Outline each blood parasite and name the species.
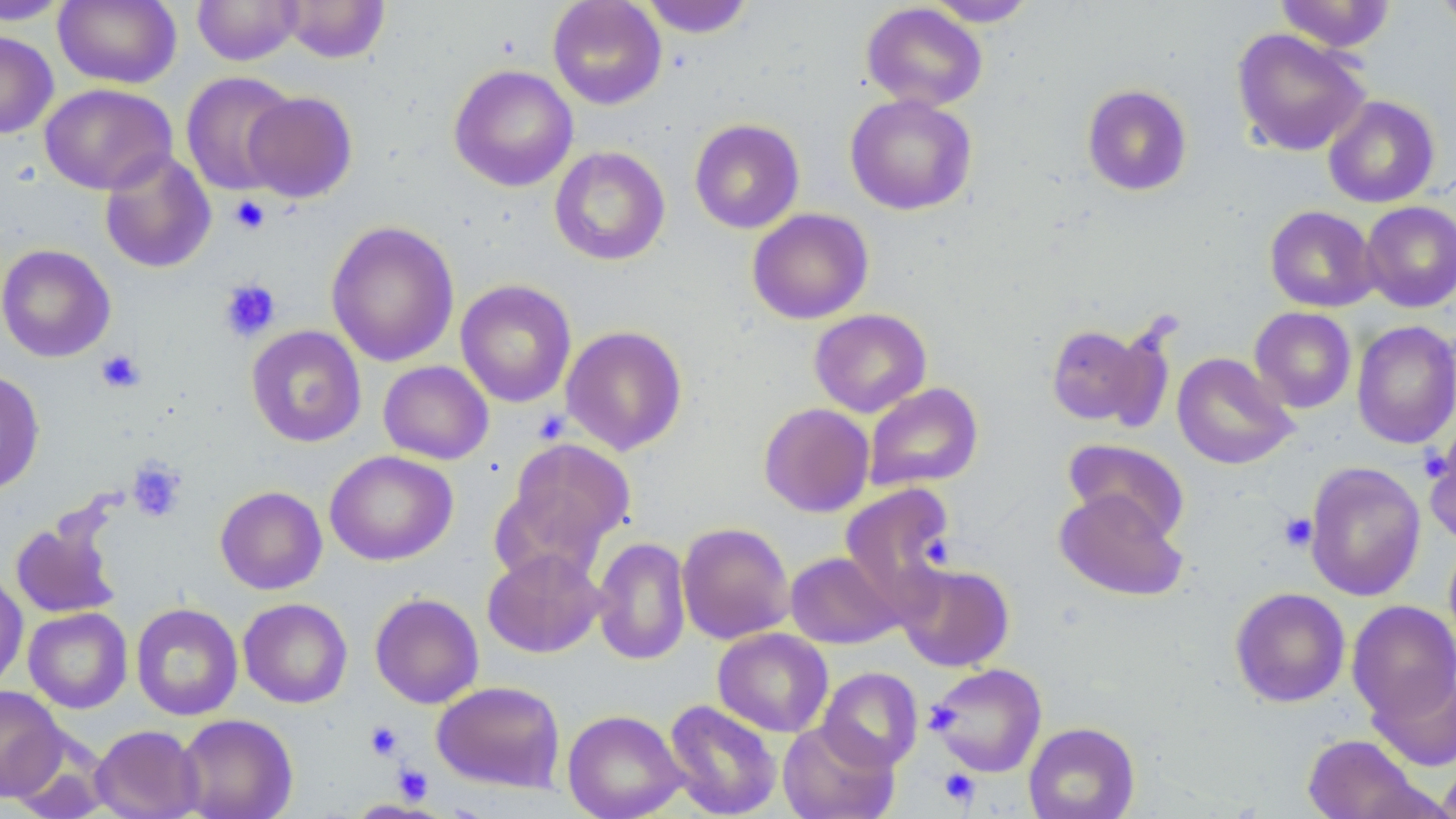

No blood parasites observed.

slide-level diagnosis = no evidence of blood parasites
platelet locations = approximate bounding boxes as (x1,y1)-(x2,y2) corner pairs in pixels: (229,196)-(271,235), (218,279)-(281,342), (96,349)-(144,394), (127,459)-(186,522), (1279,512)-(1318,552), (922,533)-(955,567), (365,720)-(404,761), (393,764)-(432,803), (938,769)-(980,808)
magnification = 1000x
uninfected red blood cell locations = approximate bounding boxes as (x1,y1)-(x2,y2) corner pairs in pixels: (54,0)-(181,88), (192,0)-(303,66), (280,0)-(390,63), (547,0)-(666,109), (638,0)-(755,38), (923,0)-(1040,26), (1275,0)-(1396,52), (1434,0)-(1456,32), (0,1)-(74,25), (861,3)-(988,111), (1231,28)-(1369,156), (0,30)-(58,139), (449,65)-(578,192), (181,71)-(298,196), (1081,83)-(1193,196), (39,84)-(178,195), (243,91)-(358,203), (845,93)-(977,215), (1322,95)-(1440,208), (689,118)-(804,234), (549,146)-(670,266), (99,150)-(216,274), (1360,201)-(1456,312), (1264,205)-(1379,312), (747,208)-(874,324), (326,221)-(460,367), (0,243)-(115,363), (455,280)-(577,407), (1249,307)-(1356,413), (809,308)-(931,417), (1351,320)-(1456,449), (1044,322)-(1168,429), (561,324)-(688,455), (246,325)-(367,447), (1172,352)-(1298,470), (378,360)-(494,465), (0,369)-(45,494), (864,382)-(984,491), (758,402)-(874,517), (1423,427)-(1456,545), (504,437)-(636,558), (1063,439)-(1190,542), (325,450)-(458,566), (1304,461)-(1426,602), (839,483)-(955,608), (215,486)-(327,595), (1054,489)-(1188,602), (10,515)-(122,620), (677,522)-(795,644), (592,537)-(691,666), (1444,537)-(1456,652), (482,548)-(605,658), (785,552)-(903,649), (896,562)-(1014,672), (0,570)-(28,691), (1229,587)-(1350,708), (369,592)-(484,708), (238,598)-(352,708), (1346,600)-(1456,721), (130,602)-(243,721), (24,607)-(133,713), (713,627)-(833,737), (926,662)-(1047,777), (818,667)-(923,771), (1368,668)-(1456,772), (431,680)-(565,792), (1,685)-(67,802), (663,699)-(782,819), (562,709)-(687,819), (175,713)-(298,819), (778,720)-(899,819), (1024,721)-(1140,819), (90,725)-(204,819), (6,733)-(115,818), (1302,734)-(1426,819), (1438,757)-(1456,819)
field of view = single
image size = 1456×819 pixels
preparation = thin blood smear
stain = May-Grünwald-Giemsa
modality = optical microscopy